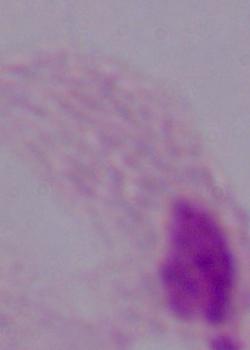

Captured at 1000x magnification. A trichomonad is shown. Micrograph.